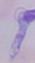

Summary:
  - Identification: trypanosome
  - Magnification: 1000x
  - Modality: photomicrograph